Comment on the morphology of the erythrocytes.
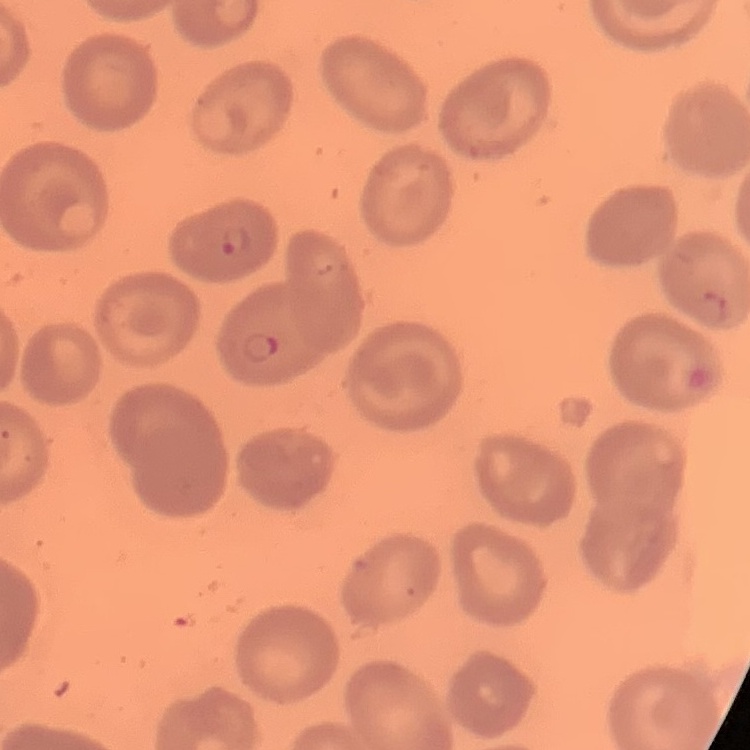
No rouleaux formation.

Field's or Giemsa stain. Square crop of a larger photomicrograph. Thin blood film.